Classify this cell by malaria status.
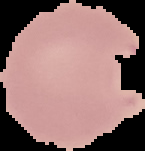

Parasitized.

Image is 145×151 pixels. From a thin blood smear. Segmented cell region on a black background.